Locate every Plasmodium falciparum-infected red blood cell.
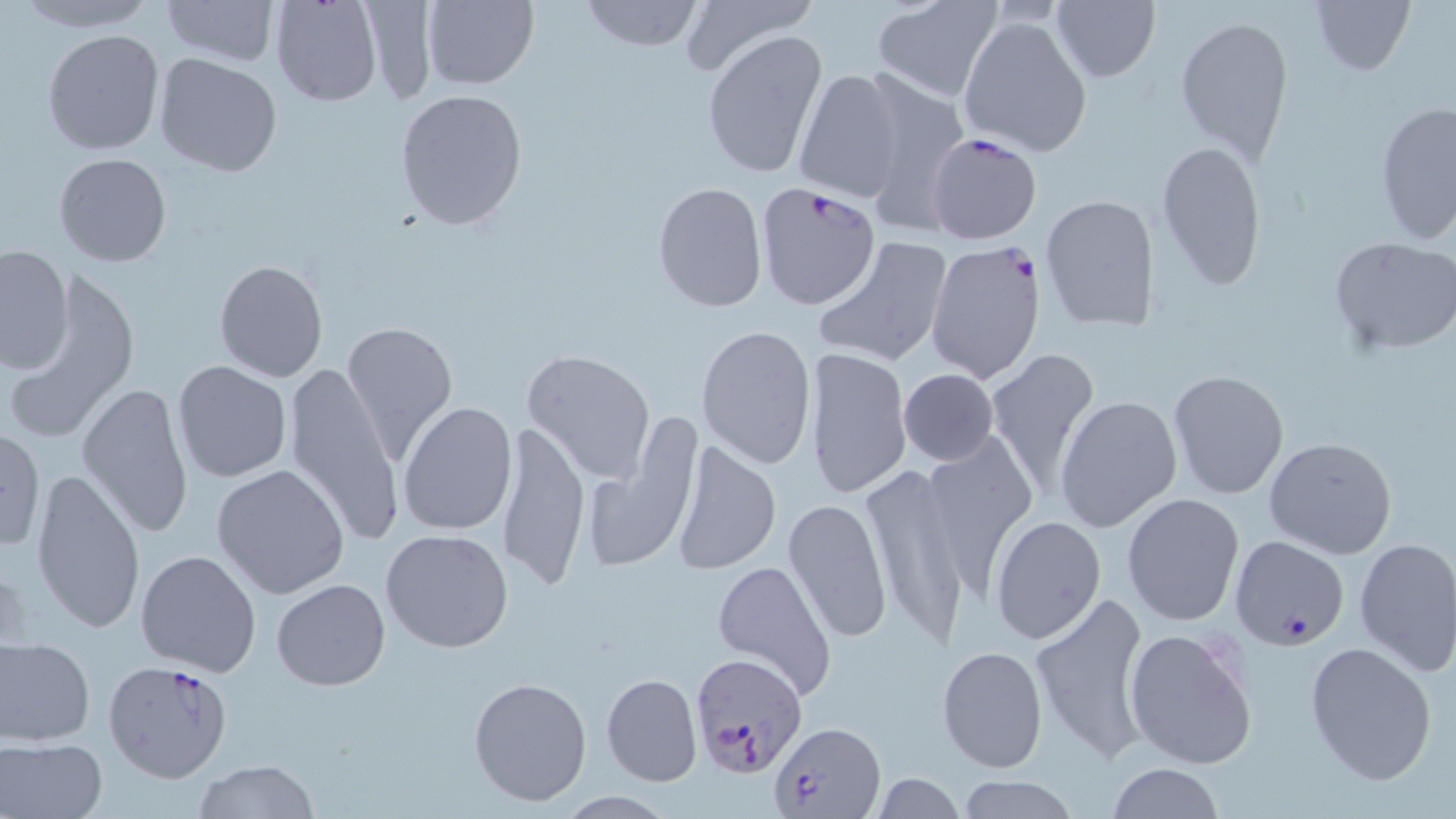

Approximate bounding boxes as named x1/y1/x2/y2 corners in pixels.
Plasmodium falciparum-infected red blood cells: (x1=925, y1=130, x2=1044, y2=246), (x1=756, y1=183, x2=881, y2=310), (x1=924, y1=240, x2=1045, y2=385), (x1=1228, y1=535, x2=1349, y2=650), (x1=689, y1=652, x2=808, y2=777), (x1=102, y1=660, x2=236, y2=784), (x1=772, y1=719, x2=885, y2=816).

Uninfected red blood cell locations: (x1=9, y1=0, x2=164, y2=34), (x1=160, y1=0, x2=279, y2=66), (x1=270, y1=0, x2=383, y2=109), (x1=360, y1=0, x2=435, y2=106), (x1=420, y1=0, x2=538, y2=90), (x1=579, y1=0, x2=705, y2=53), (x1=680, y1=0, x2=820, y2=76), (x1=869, y1=0, x2=1006, y2=103), (x1=1310, y1=0, x2=1414, y2=75), (x1=1051, y1=1, x2=1162, y2=82), (x1=959, y1=15, x2=1093, y2=159), (x1=1175, y1=15, x2=1292, y2=164), (x1=42, y1=28, x2=165, y2=157), (x1=701, y1=30, x2=827, y2=180), (x1=153, y1=52, x2=284, y2=177), (x1=791, y1=67, x2=906, y2=201), (x1=855, y1=72, x2=970, y2=227), (x1=394, y1=88, x2=529, y2=231), (x1=1375, y1=100, x2=1456, y2=247), (x1=1155, y1=139, x2=1267, y2=291), (x1=53, y1=152, x2=172, y2=268), (x1=652, y1=182, x2=768, y2=313), (x1=1038, y1=194, x2=1160, y2=332), (x1=813, y1=236, x2=953, y2=368), (x1=1328, y1=237, x2=1456, y2=354), (x1=1, y1=244, x2=75, y2=376), (x1=213, y1=260, x2=329, y2=382), (x1=8, y1=271, x2=138, y2=441), (x1=339, y1=319, x2=459, y2=465), (x1=695, y1=323, x2=817, y2=469), (x1=802, y1=346, x2=912, y2=499), (x1=983, y1=348, x2=1100, y2=499), (x1=523, y1=350, x2=655, y2=482), (x1=173, y1=360, x2=292, y2=482), (x1=280, y1=360, x2=407, y2=547), (x1=898, y1=368, x2=999, y2=467), (x1=1167, y1=369, x2=1289, y2=500), (x1=77, y1=383, x2=196, y2=537), (x1=1056, y1=395, x2=1183, y2=532), (x1=398, y1=402, x2=519, y2=537), (x1=495, y1=423, x2=588, y2=592), (x1=579, y1=425, x2=703, y2=577), (x1=0, y1=428, x2=45, y2=552), (x1=1264, y1=435, x2=1397, y2=559), (x1=670, y1=440, x2=780, y2=575), (x1=859, y1=460, x2=973, y2=652), (x1=211, y1=463, x2=350, y2=599), (x1=30, y1=468, x2=147, y2=635), (x1=1121, y1=492, x2=1245, y2=627), (x1=783, y1=498, x2=894, y2=643), (x1=990, y1=515, x2=1106, y2=645), (x1=380, y1=527, x2=515, y2=653), (x1=1353, y1=537, x2=1456, y2=676), (x1=135, y1=549, x2=262, y2=677), (x1=711, y1=559, x2=837, y2=698), (x1=271, y1=579, x2=391, y2=691), (x1=1028, y1=589, x2=1152, y2=764), (x1=1123, y1=625, x2=1258, y2=769), (x1=1, y1=635, x2=96, y2=746), (x1=1303, y1=639, x2=1438, y2=786), (x1=938, y1=646, x2=1047, y2=771), (x1=600, y1=674, x2=702, y2=787), (x1=469, y1=675, x2=592, y2=806), (x1=1, y1=736, x2=106, y2=819), (x1=194, y1=759, x2=318, y2=818), (x1=1105, y1=763, x2=1225, y2=818), (x1=869, y1=773, x2=965, y2=818), (x1=953, y1=777, x2=1082, y2=817), (x1=556, y1=791, x2=678, y2=817). Slide-level diagnosis: Plasmodium falciparum. Thin blood film. Image is 1456×819 pixels. Single field of view. Optical microscopy. 1000x magnification. May-Grünwald-Giemsa-stained preparation.